Give the extent of all uninfected red blood cells.
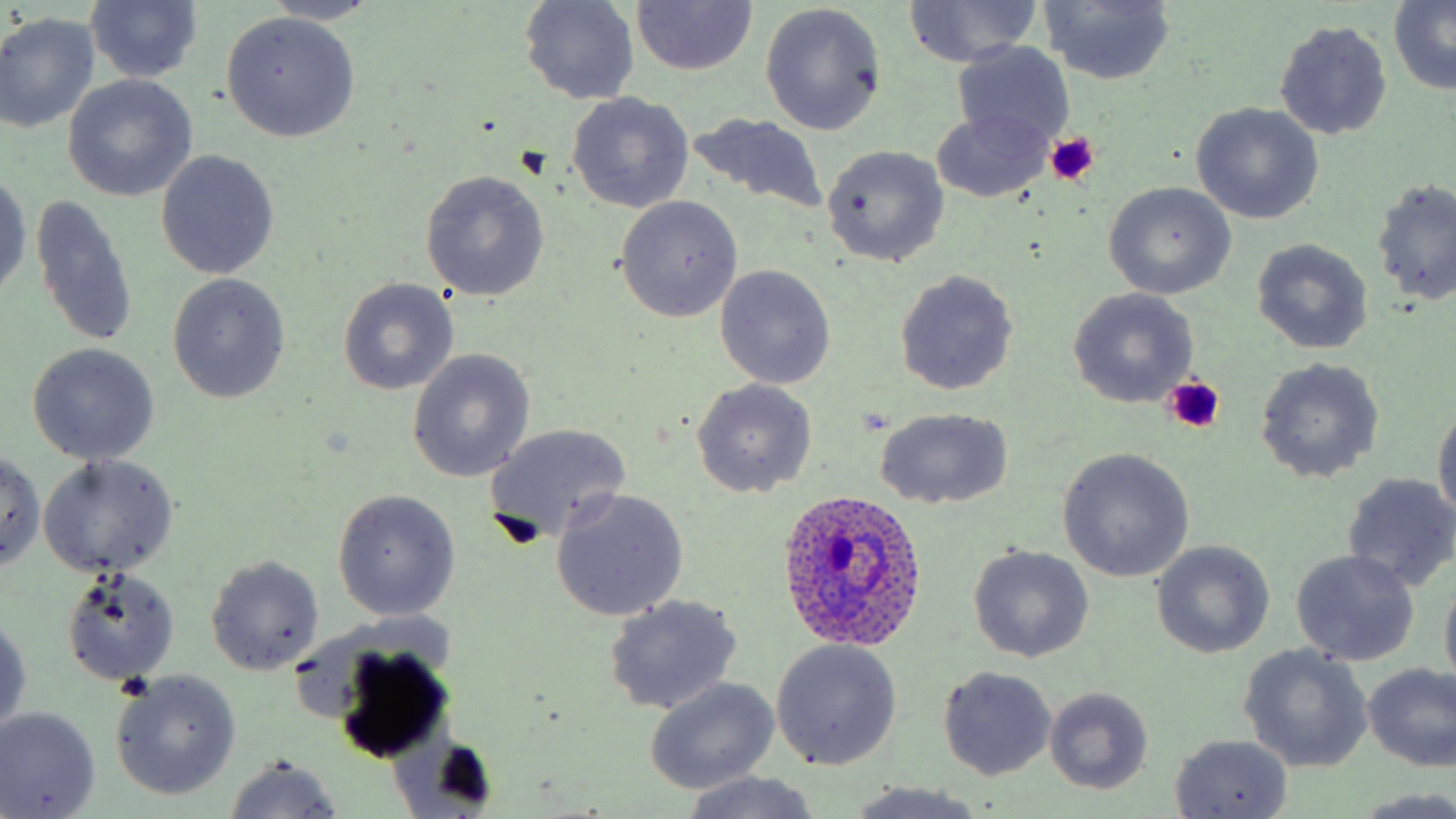

Approximate bounding boxes as named x1/y1/x2/y2 corners in pixels.
Uninfected red blood cells: (x1=264, y1=0, x2=385, y2=26), (x1=518, y1=0, x2=639, y2=106), (x1=902, y1=0, x2=1041, y2=67), (x1=631, y1=1, x2=756, y2=74), (x1=1038, y1=1, x2=1177, y2=86), (x1=1387, y1=1, x2=1456, y2=93), (x1=84, y1=2, x2=203, y2=85), (x1=761, y1=4, x2=886, y2=137), (x1=220, y1=12, x2=361, y2=142), (x1=0, y1=13, x2=100, y2=134), (x1=1274, y1=19, x2=1392, y2=141), (x1=952, y1=42, x2=1077, y2=149), (x1=4, y1=45, x2=154, y2=181), (x1=63, y1=75, x2=196, y2=201), (x1=565, y1=92, x2=695, y2=215), (x1=1192, y1=103, x2=1323, y2=224), (x1=931, y1=108, x2=1052, y2=203), (x1=682, y1=112, x2=831, y2=219), (x1=821, y1=145, x2=951, y2=267), (x1=155, y1=151, x2=279, y2=280), (x1=419, y1=170, x2=549, y2=302), (x1=1, y1=172, x2=30, y2=298), (x1=1371, y1=180, x2=1456, y2=306), (x1=1104, y1=181, x2=1237, y2=299), (x1=31, y1=195, x2=139, y2=348), (x1=614, y1=195, x2=743, y2=322), (x1=1251, y1=237, x2=1373, y2=354), (x1=715, y1=265, x2=836, y2=390), (x1=892, y1=269, x2=1019, y2=396), (x1=165, y1=273, x2=291, y2=404), (x1=338, y1=277, x2=460, y2=395), (x1=1068, y1=289, x2=1198, y2=408), (x1=26, y1=342, x2=161, y2=465), (x1=407, y1=350, x2=534, y2=483), (x1=1254, y1=357, x2=1385, y2=484), (x1=690, y1=378, x2=817, y2=498), (x1=1431, y1=401, x2=1456, y2=523), (x1=873, y1=406, x2=1015, y2=511), (x1=483, y1=423, x2=632, y2=547), (x1=1056, y1=447, x2=1194, y2=582), (x1=0, y1=452, x2=47, y2=573), (x1=38, y1=454, x2=179, y2=578), (x1=1342, y1=472, x2=1456, y2=592), (x1=331, y1=488, x2=461, y2=622), (x1=551, y1=489, x2=689, y2=620), (x1=1150, y1=540, x2=1274, y2=658), (x1=966, y1=545, x2=1094, y2=662), (x1=1291, y1=549, x2=1421, y2=666), (x1=205, y1=555, x2=324, y2=675), (x1=59, y1=567, x2=180, y2=686), (x1=1440, y1=570, x2=1456, y2=692), (x1=602, y1=595, x2=743, y2=715), (x1=1, y1=612, x2=30, y2=735), (x1=772, y1=639, x2=902, y2=771), (x1=327, y1=640, x2=455, y2=762), (x1=1238, y1=645, x2=1372, y2=774), (x1=1361, y1=662, x2=1455, y2=770), (x1=937, y1=666, x2=1058, y2=781), (x1=110, y1=671, x2=242, y2=803), (x1=644, y1=677, x2=780, y2=795), (x1=1044, y1=687, x2=1153, y2=795), (x1=0, y1=707, x2=100, y2=818), (x1=1170, y1=734, x2=1293, y2=817), (x1=224, y1=756, x2=343, y2=818), (x1=678, y1=771, x2=823, y2=818), (x1=842, y1=782, x2=990, y2=819).

Platelet locations: (x1=1044, y1=132, x2=1100, y2=185), (x1=1160, y1=378, x2=1224, y2=431). Plasmodium ovale-infected red blood cell locations: (x1=776, y1=487, x2=929, y2=650). Slide-level diagnosis: Plasmodium ovale. Single field of view. Light microscopy. 1000x magnification. May-Grünwald-Giemsa-stained preparation. Image is 1456×819 pixels. Thin blood film.